Describe the morphology of the erythrocytes.
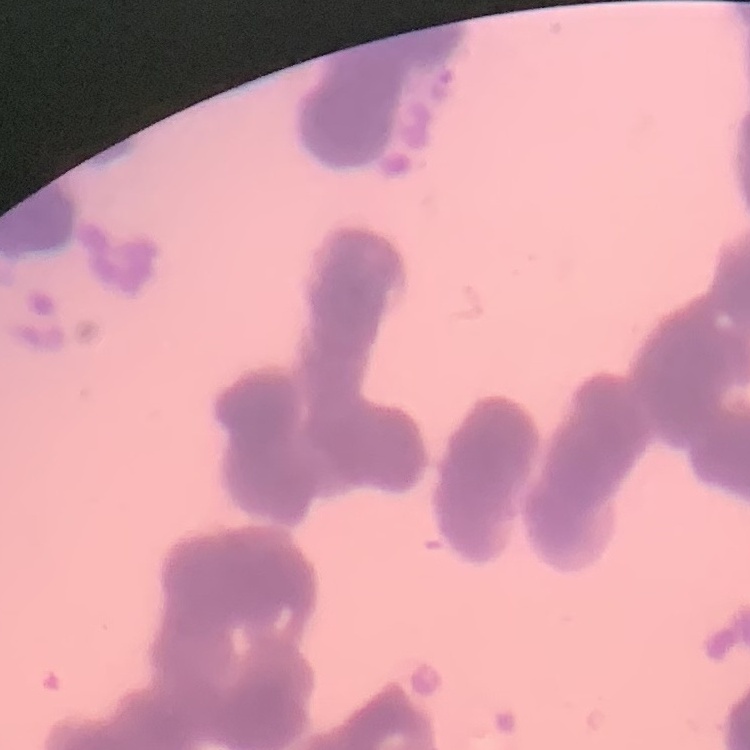
They show rouleaux formation.

image type = one tile cut from a larger photomicrograph
preparation = thin peripheral smear
stain = Field's or Giemsa